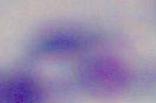

identification: Toxoplasma gondii
modality: micrograph
magnification: 1000x